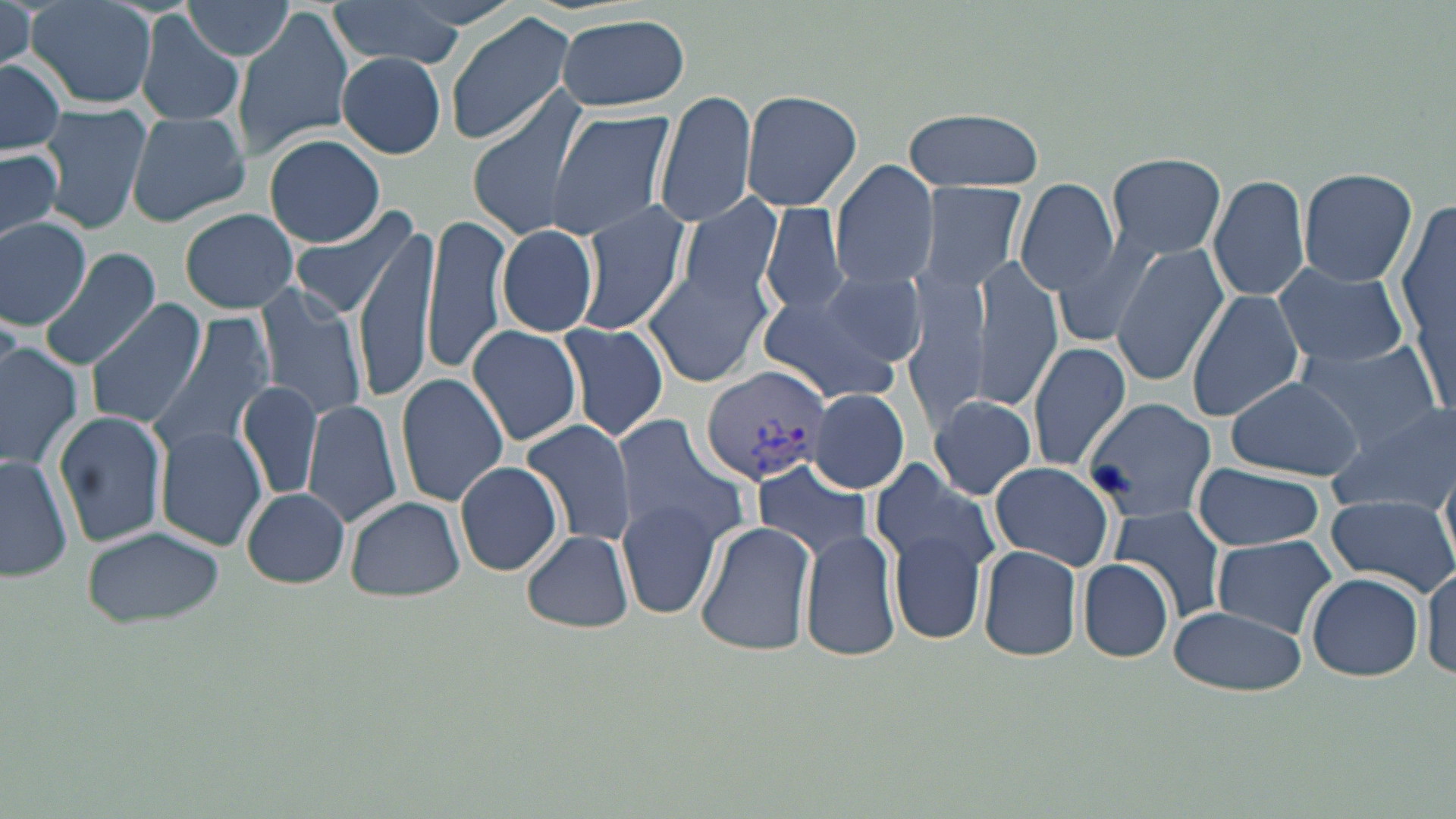 Approximate bounding boxes as named x1/y1/x2/y2 corners in pixels. Plasmodium vivax-infected red blood cell locations: (x1=697, y1=364, x2=832, y2=487). Uninfected red blood cell locations: (x1=324, y1=0, x2=471, y2=70), (x1=178, y1=1, x2=296, y2=61), (x1=0, y1=2, x2=35, y2=75), (x1=24, y1=2, x2=157, y2=109), (x1=234, y1=4, x2=353, y2=160), (x1=444, y1=12, x2=578, y2=147), (x1=136, y1=13, x2=245, y2=131), (x1=553, y1=15, x2=692, y2=113), (x1=336, y1=52, x2=446, y2=158), (x1=0, y1=58, x2=67, y2=157), (x1=738, y1=89, x2=862, y2=212), (x1=659, y1=90, x2=757, y2=231), (x1=466, y1=95, x2=589, y2=244), (x1=37, y1=104, x2=151, y2=234), (x1=901, y1=108, x2=1044, y2=193), (x1=546, y1=109, x2=678, y2=242), (x1=123, y1=110, x2=252, y2=227), (x1=261, y1=132, x2=386, y2=247), (x1=0, y1=148, x2=62, y2=246), (x1=1105, y1=151, x2=1229, y2=260), (x1=831, y1=159, x2=939, y2=291), (x1=1296, y1=166, x2=1418, y2=286), (x1=1209, y1=173, x2=1310, y2=303), (x1=912, y1=181, x2=1031, y2=298), (x1=1015, y1=181, x2=1119, y2=295), (x1=1400, y1=193, x2=1455, y2=420), (x1=676, y1=195, x2=783, y2=310), (x1=575, y1=201, x2=690, y2=334), (x1=760, y1=202, x2=850, y2=315), (x1=288, y1=204, x2=423, y2=323), (x1=178, y1=207, x2=299, y2=313), (x1=423, y1=213, x2=510, y2=375), (x1=0, y1=217, x2=94, y2=328), (x1=354, y1=220, x2=439, y2=401), (x1=495, y1=224, x2=599, y2=339), (x1=1051, y1=226, x2=1169, y2=351), (x1=1112, y1=245, x2=1230, y2=384), (x1=38, y1=246, x2=163, y2=369), (x1=968, y1=260, x2=1062, y2=411), (x1=1275, y1=261, x2=1409, y2=372), (x1=643, y1=265, x2=771, y2=387), (x1=815, y1=266, x2=929, y2=370), (x1=902, y1=272, x2=990, y2=436), (x1=255, y1=282, x2=369, y2=423), (x1=756, y1=290, x2=903, y2=404), (x1=1187, y1=291, x2=1304, y2=424), (x1=85, y1=299, x2=207, y2=428), (x1=149, y1=315, x2=274, y2=459), (x1=556, y1=322, x2=668, y2=443), (x1=466, y1=324, x2=584, y2=447), (x1=1294, y1=340, x2=1443, y2=445), (x1=1026, y1=341, x2=1133, y2=473), (x1=0, y1=344, x2=82, y2=471), (x1=395, y1=374, x2=510, y2=505), (x1=1226, y1=377, x2=1364, y2=480), (x1=237, y1=380, x2=324, y2=501), (x1=808, y1=387, x2=910, y2=494), (x1=319, y1=392, x2=492, y2=524), (x1=924, y1=395, x2=1040, y2=500), (x1=1082, y1=398, x2=1215, y2=523), (x1=301, y1=399, x2=404, y2=528), (x1=1327, y1=402, x2=1456, y2=516), (x1=54, y1=409, x2=169, y2=547), (x1=611, y1=415, x2=750, y2=545), (x1=521, y1=419, x2=637, y2=548), (x1=153, y1=426, x2=266, y2=551), (x1=0, y1=451, x2=74, y2=583), (x1=752, y1=459, x2=875, y2=562), (x1=452, y1=460, x2=564, y2=576), (x1=987, y1=461, x2=1113, y2=568), (x1=871, y1=463, x2=1004, y2=583), (x1=1193, y1=463, x2=1326, y2=551), (x1=240, y1=487, x2=350, y2=588), (x1=1324, y1=491, x2=1455, y2=596), (x1=345, y1=496, x2=465, y2=602), (x1=616, y1=496, x2=725, y2=621), (x1=1104, y1=503, x2=1231, y2=623), (x1=695, y1=521, x2=816, y2=658), (x1=81, y1=526, x2=226, y2=631), (x1=801, y1=529, x2=903, y2=664), (x1=889, y1=529, x2=988, y2=643), (x1=521, y1=530, x2=632, y2=634), (x1=1211, y1=534, x2=1337, y2=637), (x1=976, y1=542, x2=1085, y2=663), (x1=1078, y1=558, x2=1175, y2=664), (x1=1423, y1=558, x2=1456, y2=682), (x1=1305, y1=573, x2=1425, y2=681), (x1=1168, y1=604, x2=1308, y2=697). Slide-level diagnosis: Plasmodium vivax. Optical microscopy. Image is 1456×819 pixels. May-Grünwald-Giemsa stain. Thin blood film. Single field of view. Captured at 1000x magnification.